Classify this cell by malaria status.
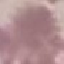
It is uninfected.

Summary:
  - Capture: smartphone through the microscope eyepiece
  - Image type: cell patch, automatically extracted from a larger field of view and resized to 64 × 64 pixels
  - Preparation: thin blood smear
  - Stain: Giemsa